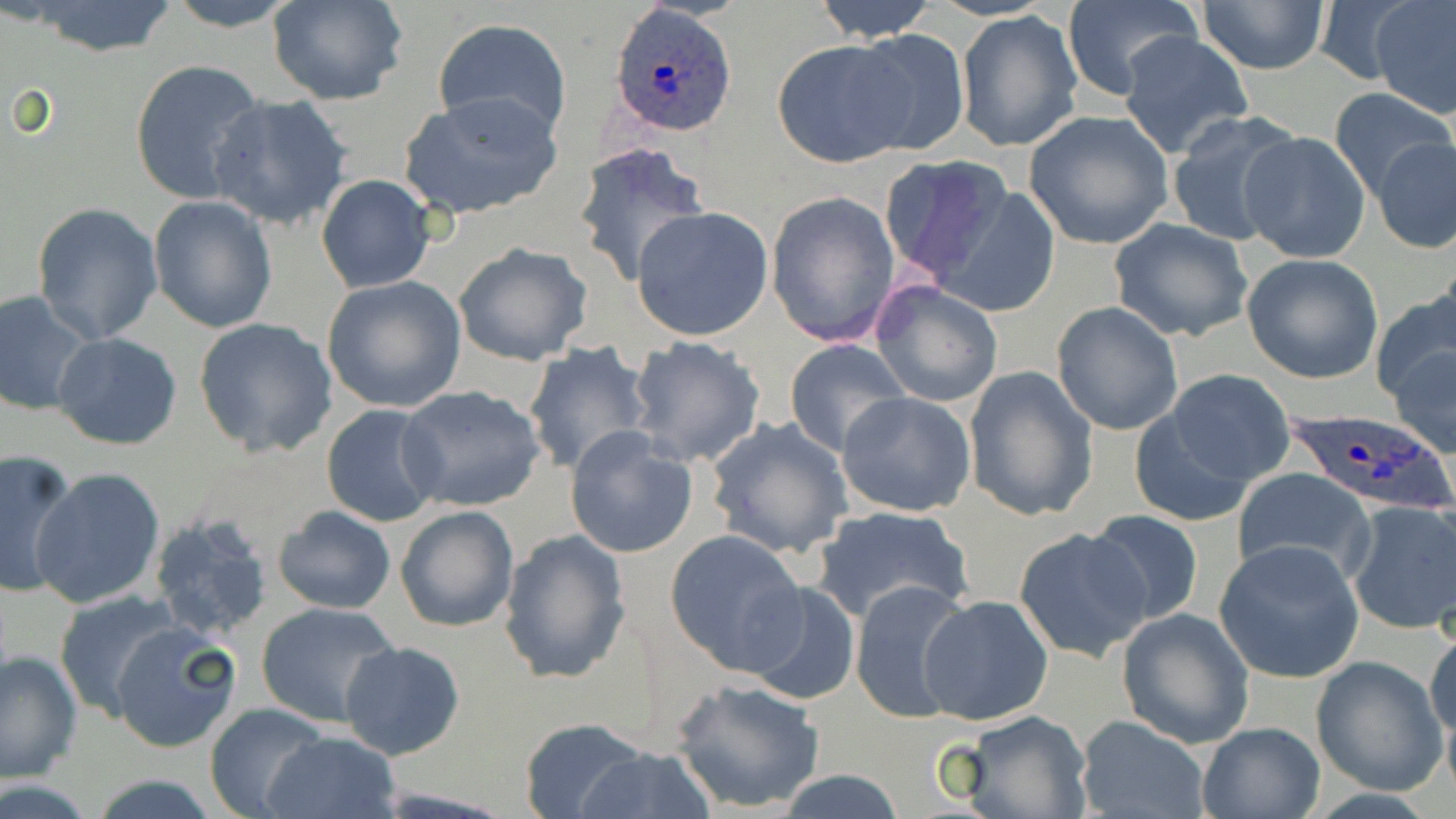 Approximate bounding boxes as (x1,y1)-(x2,y2) corner pairs in pixels. Uninfected red blood cell locations: (160,0)-(305,30), (268,0)-(408,105), (812,0)-(939,41), (1312,1)-(1421,86), (1371,1)-(1456,118), (25,2)-(179,57), (1060,2)-(1201,101), (1196,2)-(1330,74), (956,12)-(1083,153), (431,17)-(573,139), (846,29)-(972,158), (1118,32)-(1254,159), (772,38)-(916,167), (129,58)-(266,205), (1328,87)-(1455,199), (399,91)-(565,222), (204,92)-(355,231), (1023,110)-(1174,249), (1165,111)-(1302,248), (1236,131)-(1372,264), (1372,137)-(1455,255), (573,141)-(708,288), (877,154)-(1014,285), (316,174)-(436,293), (930,185)-(1065,317), (765,190)-(901,349), (148,196)-(278,334), (31,201)-(165,345), (630,206)-(773,342), (1109,218)-(1254,342), (453,241)-(593,367), (1242,253)-(1385,383), (320,276)-(467,413), (870,280)-(1004,408), (1373,286)-(1456,411), (0,291)-(97,417), (1050,300)-(1184,436), (193,317)-(338,458), (53,332)-(183,449), (626,335)-(768,469), (784,338)-(910,456), (1387,338)-(1456,459), (521,342)-(654,475), (962,365)-(1099,523), (1155,369)-(1293,490), (396,384)-(548,511), (837,391)-(980,518), (1126,399)-(1264,526), (321,403)-(446,527), (706,416)-(855,560), (564,427)-(699,559), (0,451)-(81,599), (29,467)-(165,610), (1231,468)-(1377,586), (1345,501)-(1456,636), (272,504)-(397,615), (395,504)-(520,634), (811,504)-(971,625), (1083,509)-(1207,627), (147,512)-(275,641), (1014,526)-(1152,662), (498,529)-(631,685), (665,529)-(807,674), (1213,540)-(1366,683), (850,579)-(976,728), (741,580)-(862,706), (54,590)-(186,721), (919,593)-(1054,725), (254,601)-(396,727), (1116,608)-(1255,749), (108,622)-(242,754), (1425,623)-(1455,758), (339,640)-(465,761), (0,648)-(82,785), (1310,655)-(1447,795), (671,678)-(825,814), (205,703)-(331,818), (960,711)-(1093,819), (1075,715)-(1210,819), (519,716)-(649,818), (1195,721)-(1325,818), (266,729)-(399,819), (574,745)-(715,818), (774,770)-(910,819), (88,775)-(225,817). Plasmodium ovale-infected red blood cell locations: (609,4)-(735,138), (1285,408)-(1454,520). Slide-level diagnosis: Plasmodium ovale. Thin blood smear. Light microscopy. Image is 1456×819 pixels. 1000x magnification. May-Grünwald-Giemsa-stained preparation. Single field of view.